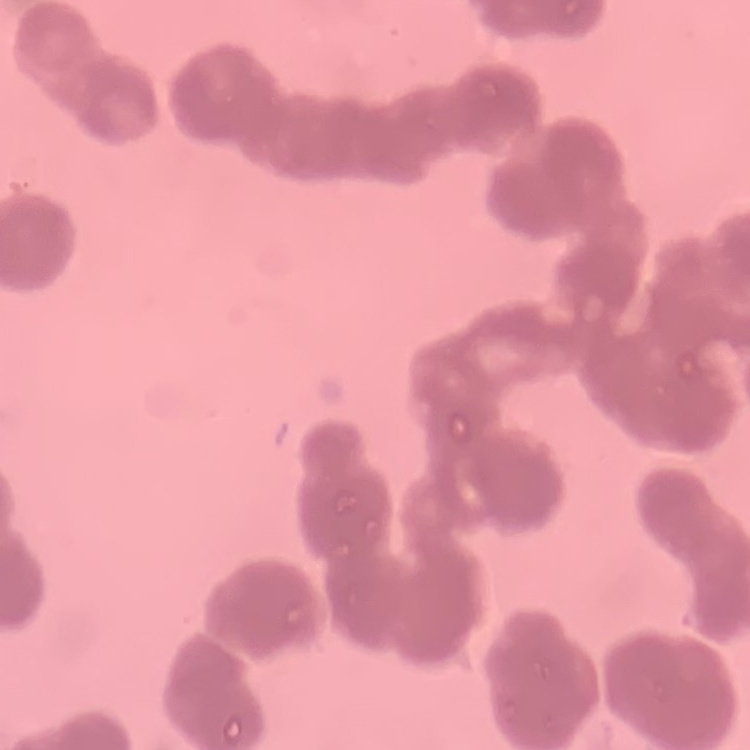
Summary:
  - Red blood cell morphology: rouleaux formation
  - Image type: one tile cut from a larger photomicrograph
  - Stain: Field's or Giemsa
  - Preparation: thin peripheral smear